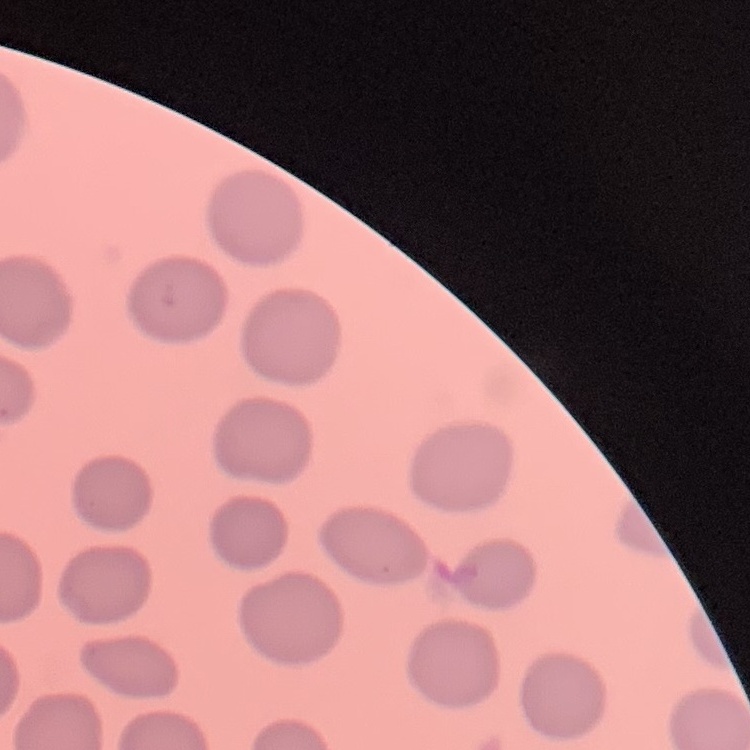
Summary:
  - Erythrocyte morphology: no rouleaux formation
  - Image type: square crop of a larger photomicrograph
  - Stain: Field's or Giemsa
  - Preparation: thin blood smear